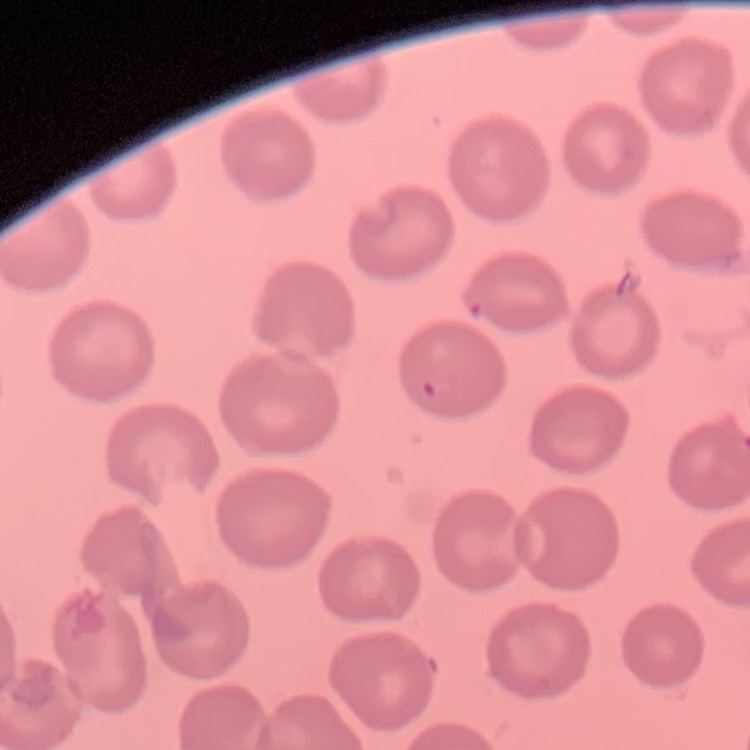
erythrocyte morphology = no rouleaux formation
preparation = thin blood film
image type = square crop of a larger photomicrograph
stain = Field's or Giemsa